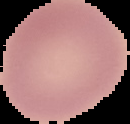
result = no Plasmodium parasites detected
preparation = thin blood film
image type = segmented cell region on a black background
image size = 130×124 pixels